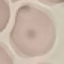 Malaria status: uninfected. Thin smear of blood. Giemsa-stained preparation. Acquired by smartphone through the microscope eyepiece. Cell patch, automatically extracted from a larger field of view and resized to 64 × 64 pixels.